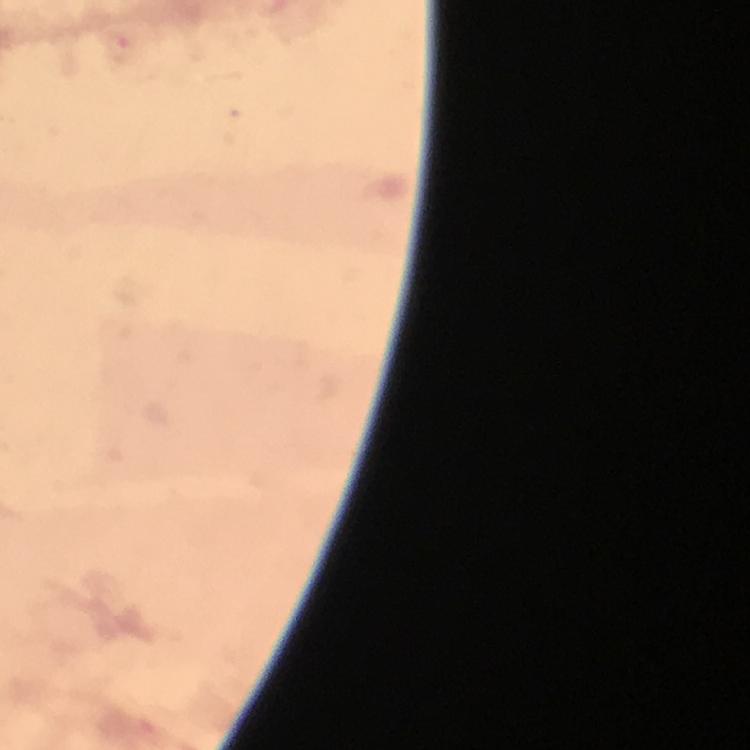

Approximate centers as [x, y] in pixels. Malaria parasite locations: [122, 46]. Photographed with a smartphone mounted on the microscope. Thick smear. From a diagnostic examination for malaria. Immersion oil was used. A crop from one field of view. Giemsa stain. Image is 750×750 pixels. At 100x magnification.